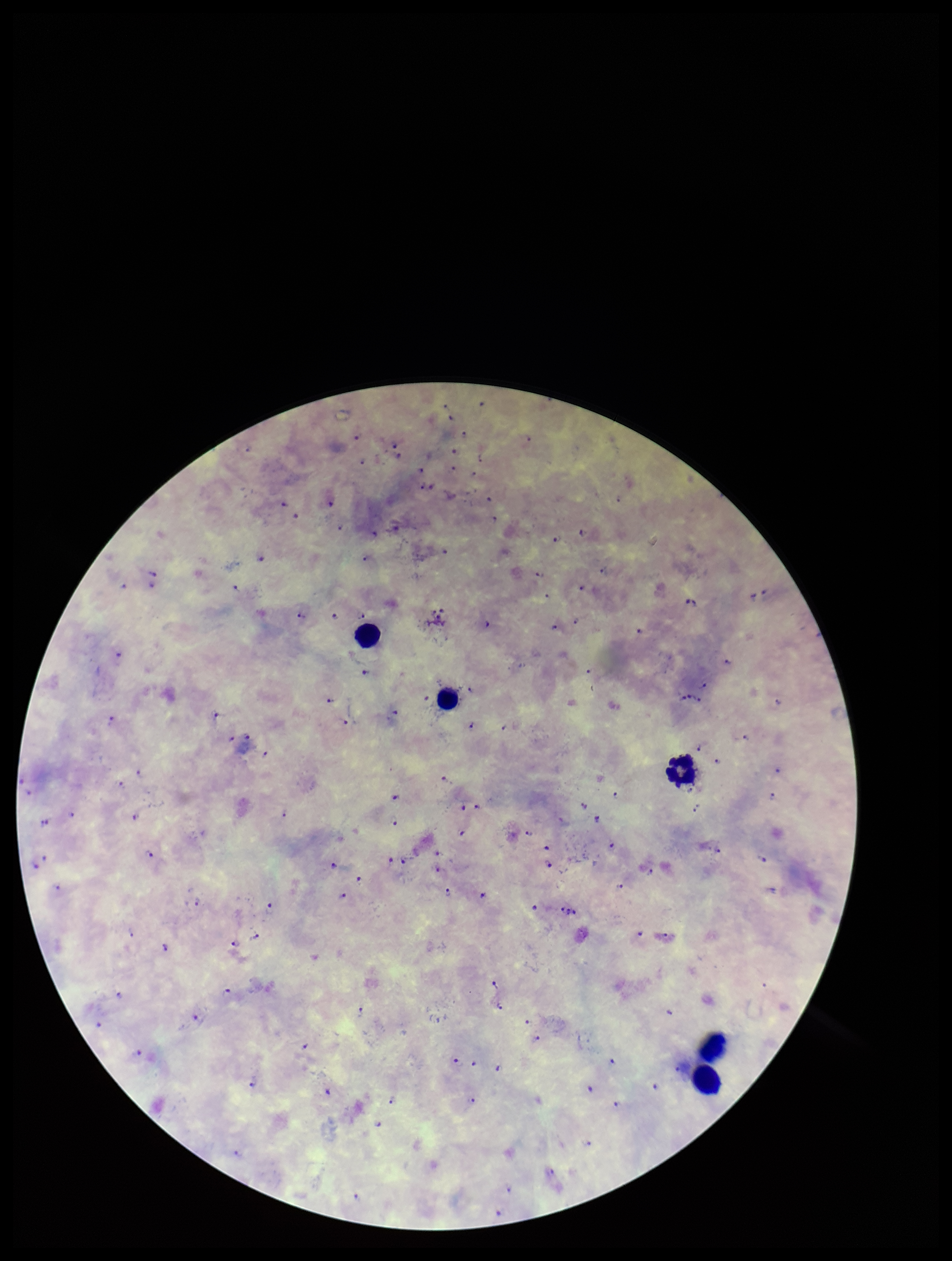

Summary:
  - Leukocyte count: 5
  - Stain: Giemsa
  - Preparation: thick smear
  - Capture: smartphone photograph through the microscope eyepiece
  - Field of view: one from this slide
  - Image size: 952×1261 pixels
  - Species reported for this patient: Plasmodium falciparum
  - Patient malaria status: infected
  - Parasite count: 89
  - Plasmodium parasites: seen